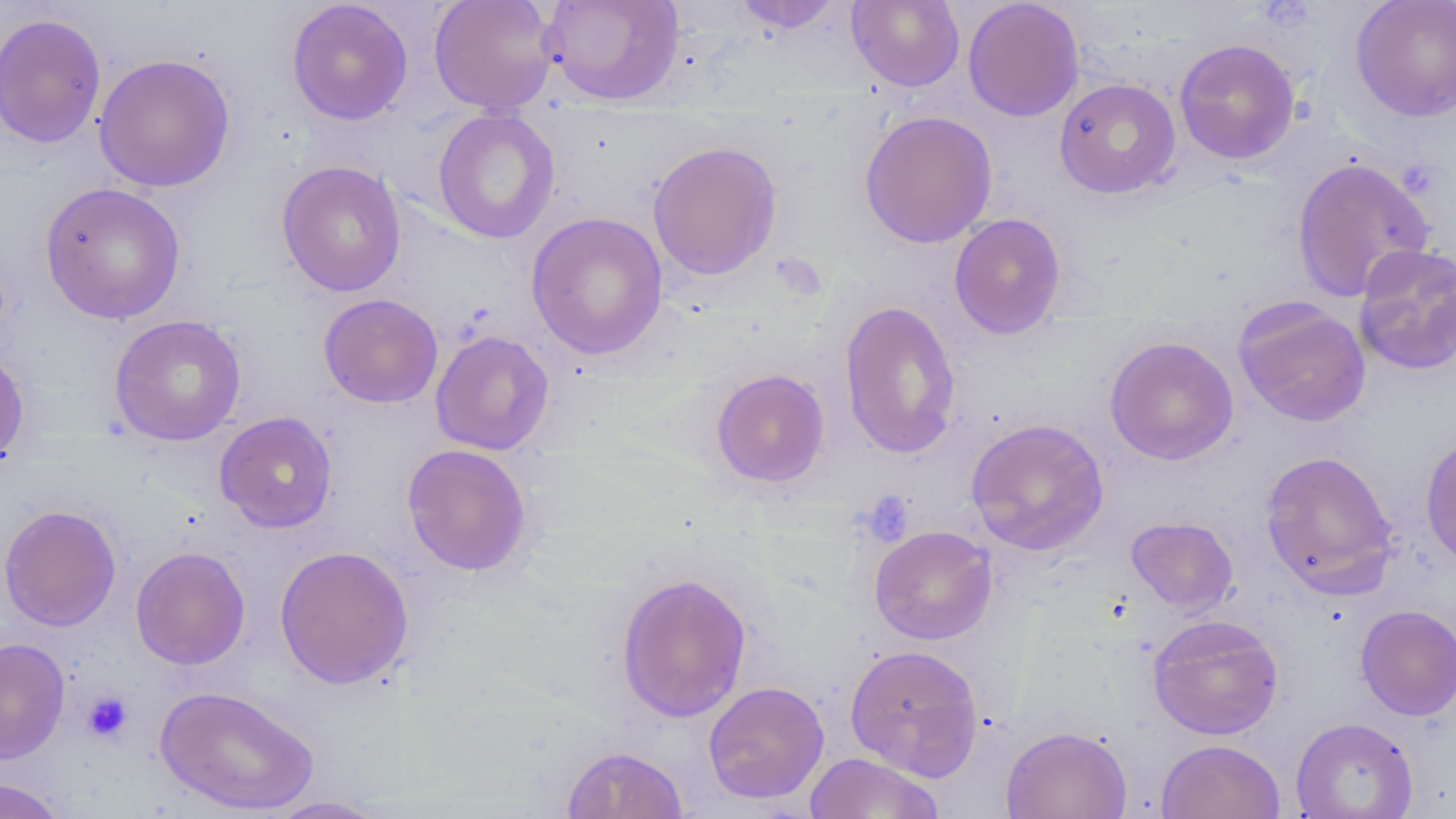

Summary:
  - Coordinate format: approximate bounding boxes as [x1, y1, x2, y2] in pixels
  - Platelet locations: [858, 491, 914, 546], [81, 690, 134, 743]
  - Uninfected red blood cell locations: [429, 0, 559, 115], [542, 0, 685, 105], [846, 0, 965, 92], [962, 0, 1084, 122], [286, 1, 414, 126], [730, 1, 846, 35], [1350, 1, 1456, 121], [0, 12, 106, 149], [1174, 38, 1300, 165], [93, 53, 236, 192], [1054, 78, 1181, 199], [432, 108, 561, 244], [858, 110, 997, 249], [646, 139, 783, 281], [1291, 156, 1434, 302], [276, 160, 407, 297], [39, 181, 186, 325], [525, 212, 669, 360], [949, 213, 1067, 340], [1352, 242, 1456, 376], [318, 293, 443, 408], [1233, 298, 1371, 428], [839, 299, 962, 459], [108, 314, 247, 446], [430, 330, 555, 455], [1104, 336, 1239, 465], [0, 347, 30, 467], [710, 368, 830, 488], [214, 411, 338, 533], [966, 418, 1110, 556], [1420, 434, 1456, 569], [402, 444, 532, 576], [1259, 450, 1398, 597], [0, 504, 122, 632], [1125, 516, 1239, 616], [869, 525, 998, 645], [274, 544, 414, 690], [130, 545, 251, 670], [615, 571, 753, 723], [1355, 605, 1456, 720], [1147, 614, 1284, 740], [0, 637, 70, 763], [844, 644, 984, 779], [703, 680, 829, 804], [154, 685, 320, 816], [1291, 717, 1418, 818], [1001, 725, 1132, 819], [1156, 739, 1285, 819], [561, 744, 688, 819], [804, 752, 945, 819], [0, 778, 66, 819], [264, 795, 394, 818]
  - Slide-level diagnosis: no evidence of blood parasites
  - Stain: May-Grünwald-Giemsa
  - Magnification: 1000x
  - Modality: optical microscopy
  - Image size: 1456×819 pixels
  - Preparation: thin blood film
  - Field of view: one of a larger specimen